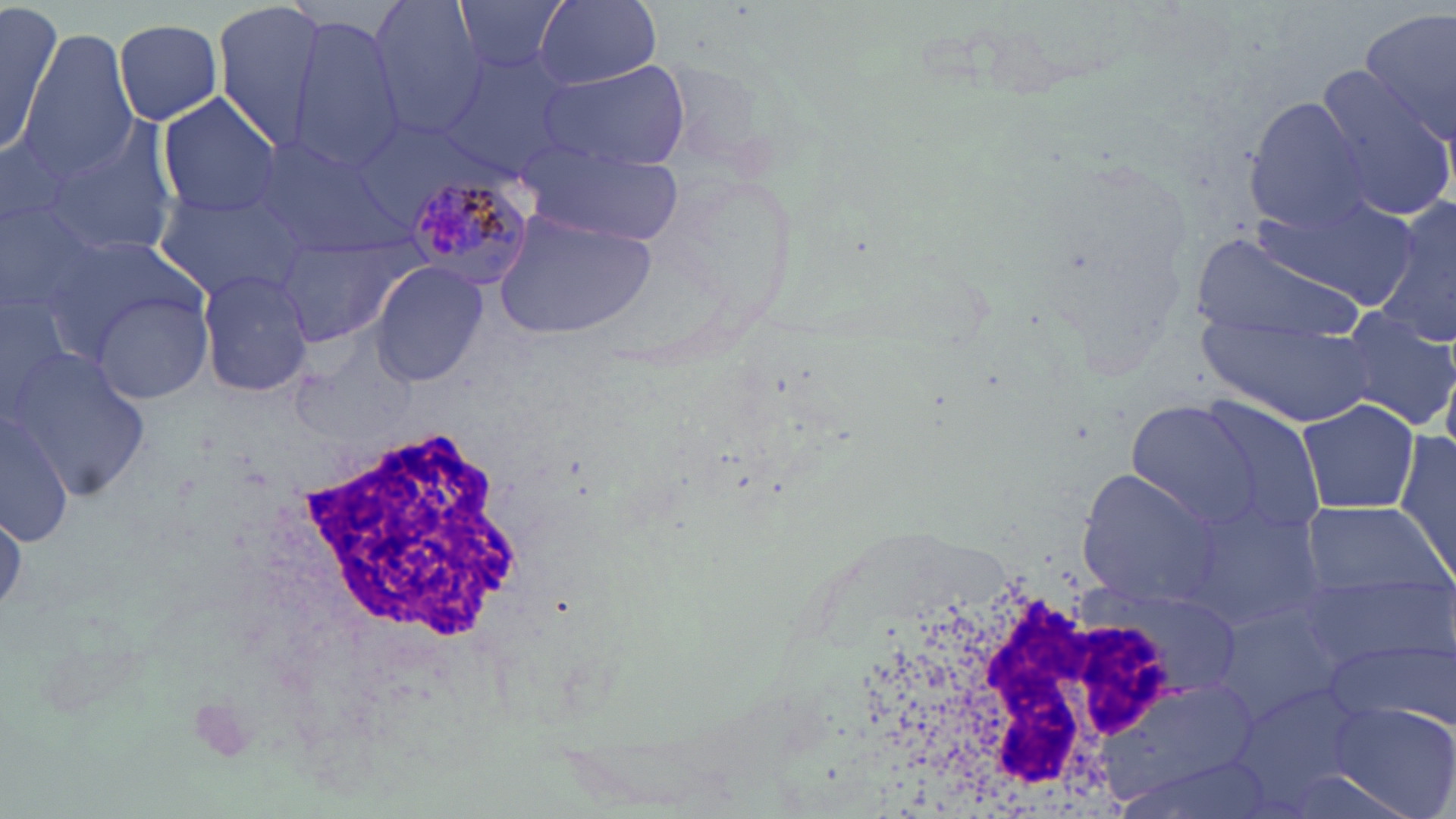 Approximate bounding boxes as (x1, y1, x2, y2) in pixels. Uninfected red blood cell locations: (450, 0, 575, 76), (536, 0, 662, 89), (213, 1, 333, 151), (369, 1, 486, 138), (0, 5, 63, 160), (1360, 7, 1456, 142), (112, 17, 224, 125), (283, 18, 407, 172), (23, 31, 141, 176), (438, 49, 586, 178), (537, 61, 687, 169), (1313, 72, 1455, 220), (157, 93, 284, 218), (1243, 96, 1376, 230), (48, 113, 183, 261), (252, 137, 410, 261), (523, 140, 682, 247), (154, 184, 314, 304), (1255, 194, 1415, 306), (0, 199, 108, 322), (1376, 201, 1456, 348), (496, 208, 655, 341), (1190, 230, 1368, 349), (279, 233, 410, 344), (50, 236, 204, 353), (370, 261, 487, 387), (196, 269, 316, 397), (0, 290, 89, 421), (92, 291, 213, 404), (1340, 306, 1455, 434), (1195, 310, 1375, 424), (5, 349, 156, 503), (1124, 394, 1317, 541), (1293, 396, 1422, 517), (0, 406, 78, 548), (1396, 426, 1456, 585), (1076, 469, 1226, 607), (1180, 497, 1324, 628), (1296, 501, 1447, 595), (1, 502, 24, 620), (1298, 566, 1455, 673), (1212, 601, 1355, 724), (1326, 638, 1454, 730), (1232, 680, 1376, 804), (1325, 701, 1456, 819). Plasmodium malariae-infected red blood cell locations: (400, 175, 535, 293). White blood cell locations: (212, 417, 549, 764), (840, 559, 1196, 812). Slide-level diagnosis: Plasmodium malariae. Image is 1456×819 pixels. May-Grünwald-Giemsa-stained preparation. Single field of view. Thin blood smear. Light microscopy. 1000x magnification.